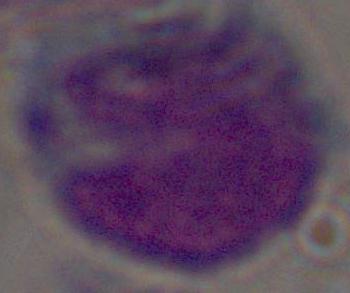
magnification = 1000x
modality = micrograph
identification = white blood cell